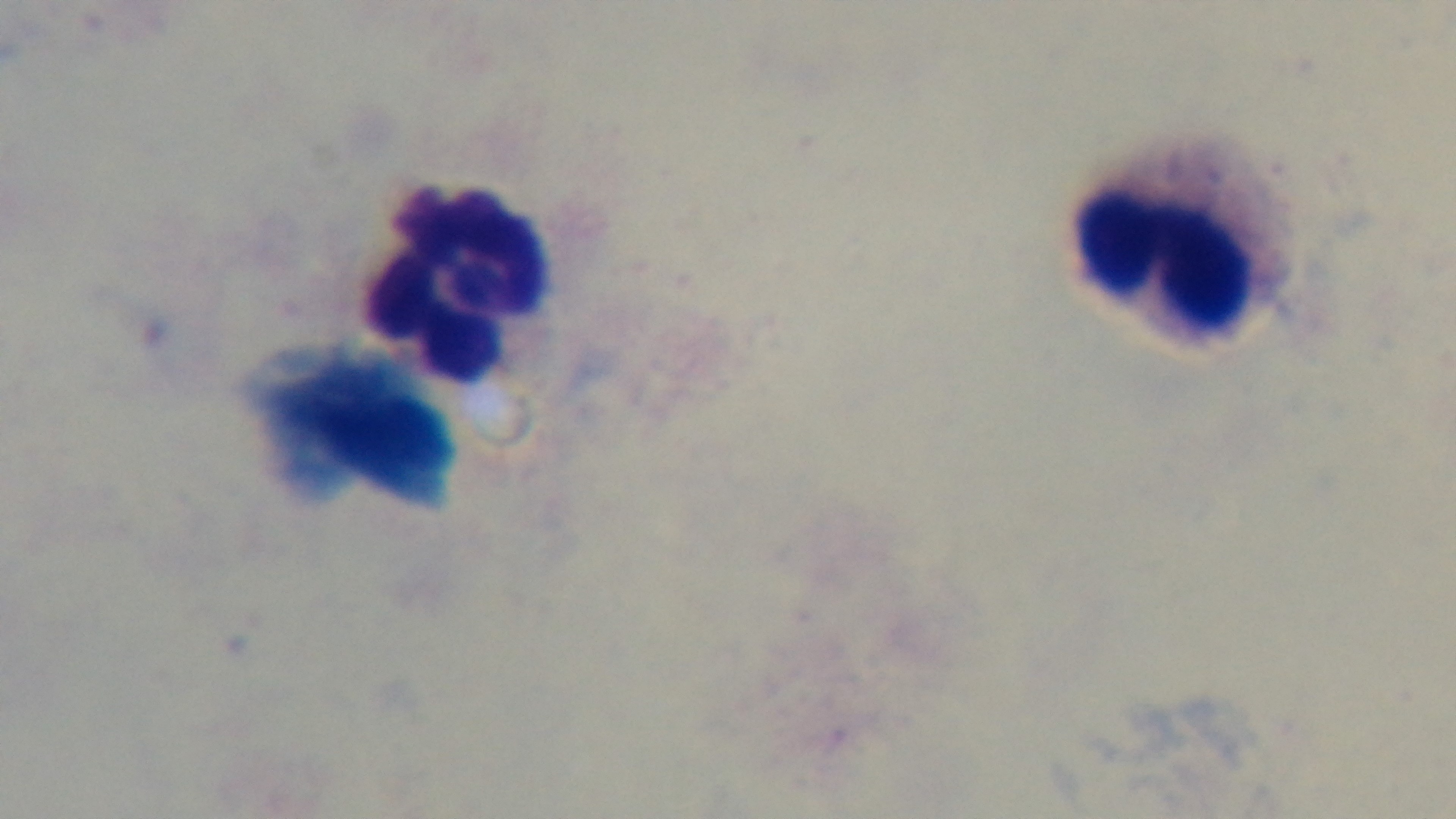

Summary:
  - Modality: light microscopy
  - Capture: mounted 4K digital camera
  - Field of view: single
  - Preparation: thick
  - Malaria status: negative
  - Objective: 100x oil immersion
  - Stain: Giemsa